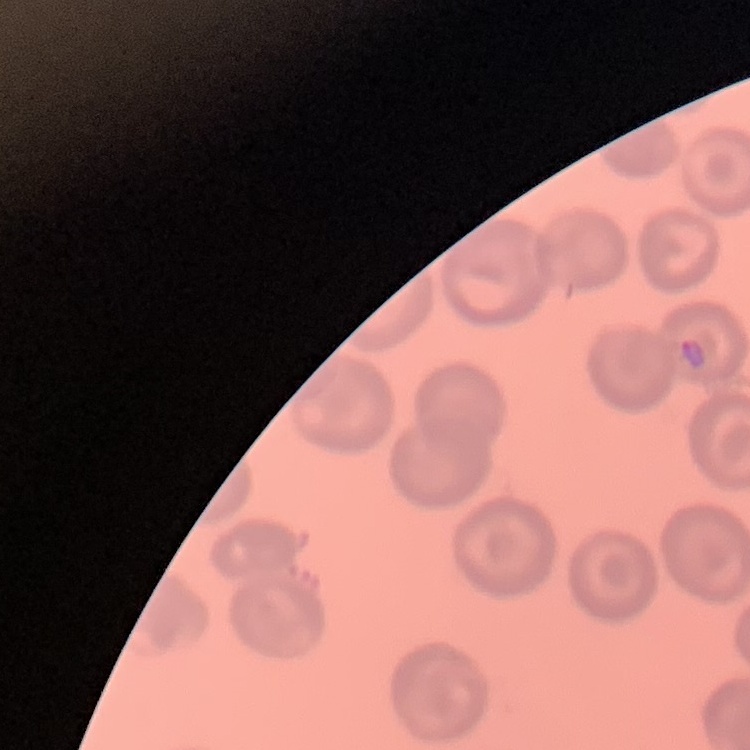
{
  "red_blood_cell_morphology": "no rouleaux formation",
  "stain": "Field's or Giemsa",
  "image_type": "square crop of a larger photomicrograph",
  "preparation": "thin peripheral smear"
}